Locate every Plasmodium parasite.
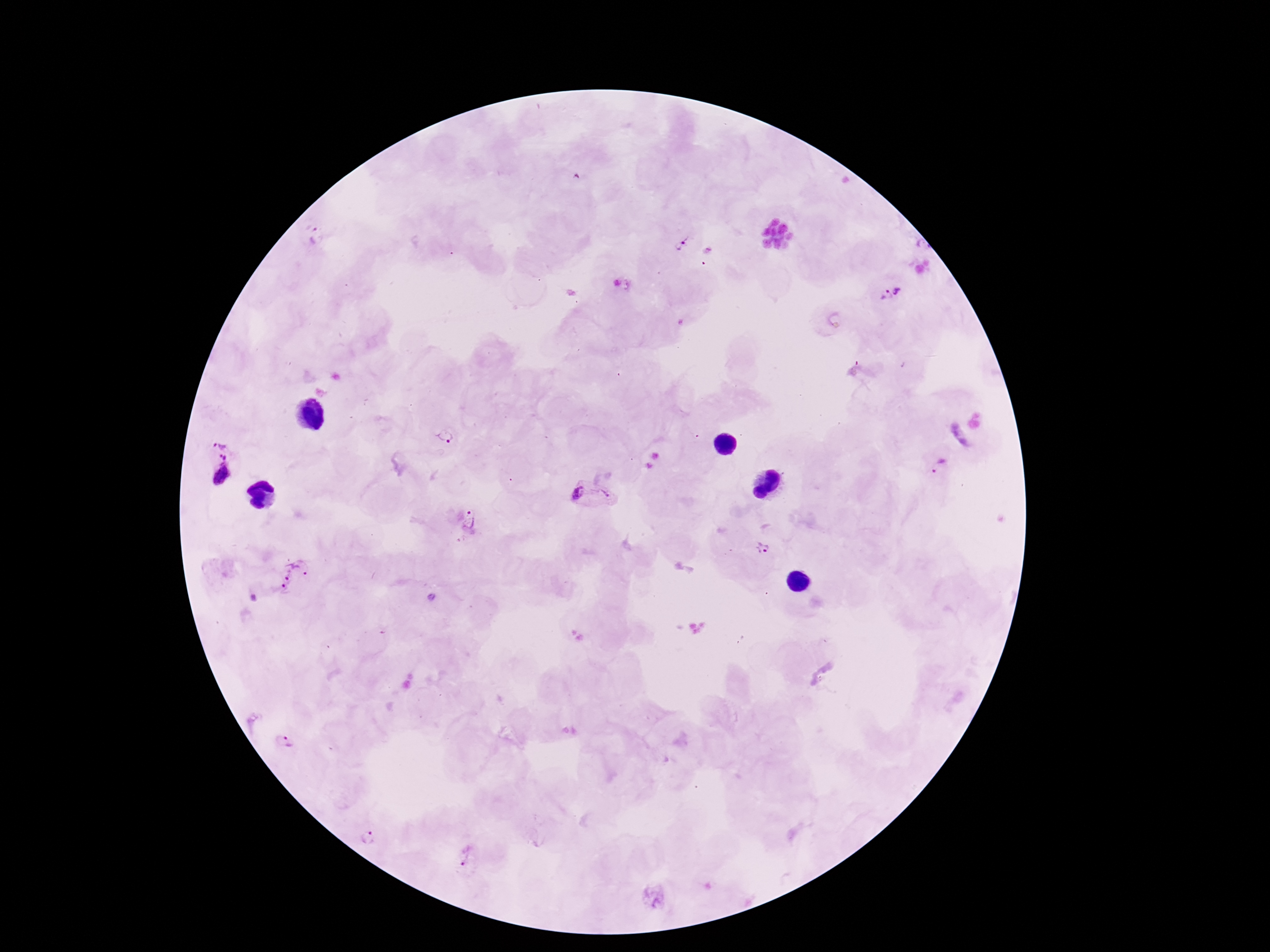

Approximate object centers, in pixels from the top-left corner.
Plasmodium parasites: (x=314, y=236), (x=684, y=244), (x=900, y=291), (x=883, y=296), (x=445, y=436), (x=222, y=438), (x=224, y=456), (x=941, y=466), (x=222, y=479), (x=575, y=493), (x=608, y=495), (x=469, y=520), (x=763, y=548), (x=292, y=574), (x=285, y=741), (x=368, y=837), (x=467, y=854).

Image is 1270×952 pixels. 100x magnification. Photographed through the microscope eyepiece with a smartphone camera. Patient malaria status: infected. One field from this slide. Thick blood smear. Giemsa-stained preparation.